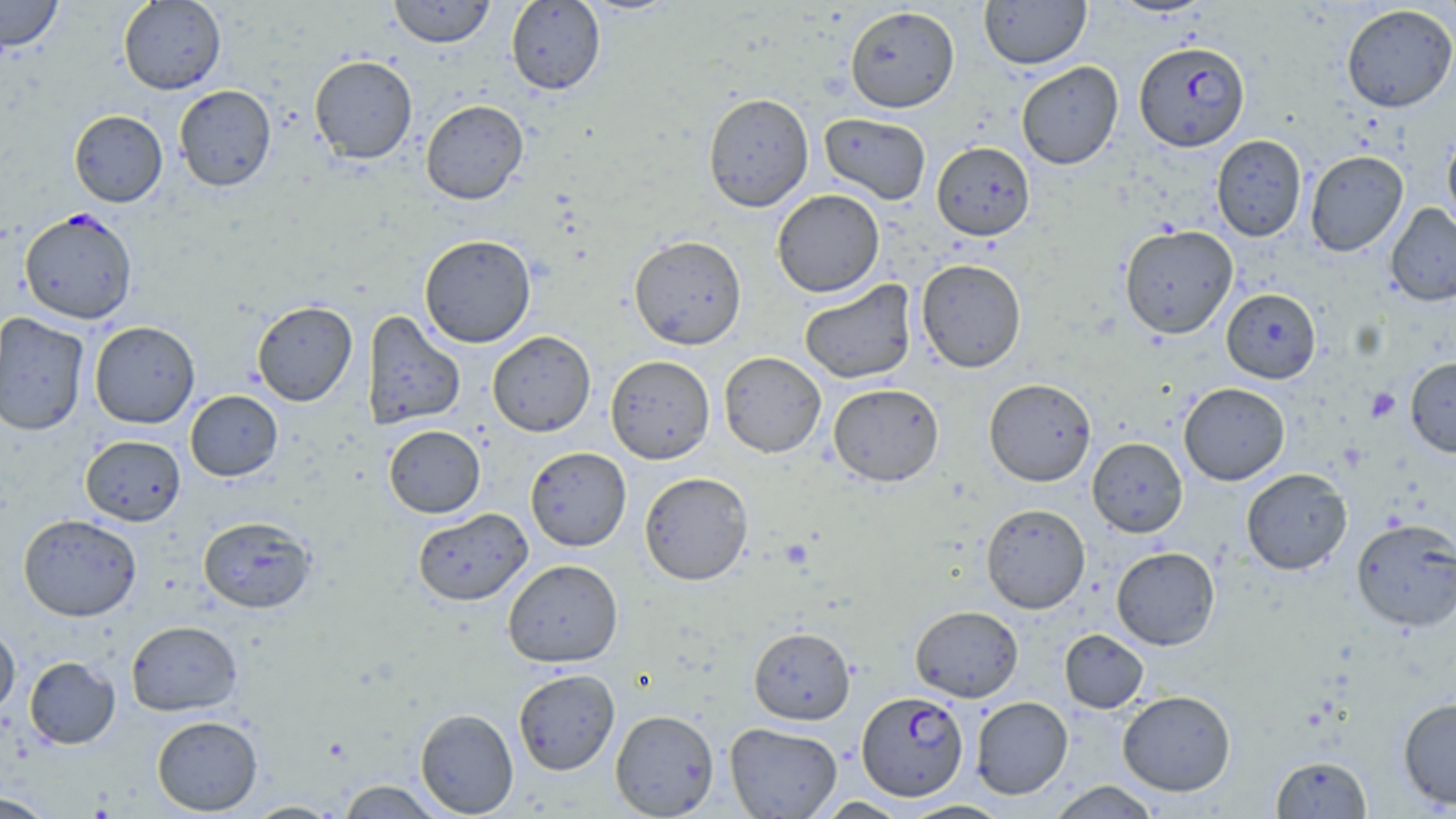

Approximate bounding boxes as [x1, y1, x2, y2] in pixels. Platelet locations: [1366, 388, 1401, 422]. Plasmodium falciparum-infected red blood cell locations: [1134, 42, 1250, 152], [19, 208, 137, 324], [856, 691, 969, 801]. Uninfected red blood cell locations: [0, 0, 63, 53], [118, 0, 226, 94], [388, 0, 496, 48], [506, 0, 606, 95], [576, 0, 683, 16], [979, 0, 1091, 69], [1108, 0, 1215, 18], [1439, 0, 1456, 39], [1341, 4, 1455, 113], [845, 6, 960, 113], [309, 55, 418, 164], [1016, 61, 1123, 169], [173, 85, 277, 192], [703, 92, 814, 212], [420, 99, 529, 204], [69, 110, 167, 207], [819, 113, 931, 204], [1442, 128, 1456, 232], [1211, 135, 1307, 241], [931, 141, 1034, 239], [1305, 150, 1408, 256], [772, 189, 884, 297], [1386, 203, 1456, 306], [1119, 225, 1238, 339], [419, 234, 536, 348], [628, 235, 747, 350], [916, 258, 1027, 373], [799, 279, 916, 384], [1221, 288, 1321, 383], [251, 300, 357, 406], [362, 310, 466, 430], [0, 313, 90, 437], [89, 321, 200, 428], [487, 330, 596, 437], [719, 351, 826, 458], [605, 355, 715, 464], [1405, 357, 1456, 457], [984, 378, 1096, 486], [1179, 382, 1290, 485], [828, 383, 944, 487], [185, 390, 282, 481], [384, 425, 485, 517], [80, 435, 186, 525], [1087, 437, 1187, 537], [525, 446, 631, 551], [1241, 468, 1352, 575], [639, 471, 753, 585], [981, 503, 1091, 614], [413, 508, 532, 605], [18, 514, 142, 621], [198, 516, 317, 614], [1351, 518, 1456, 632], [1111, 546, 1220, 650], [502, 558, 624, 668], [910, 605, 1024, 702], [126, 620, 243, 716], [0, 625, 20, 716], [748, 626, 855, 724], [1060, 629, 1148, 713], [24, 656, 120, 749], [513, 668, 620, 775], [1117, 690, 1236, 796], [971, 696, 1072, 799], [1398, 697, 1456, 810], [415, 708, 518, 817], [610, 709, 719, 818], [152, 715, 263, 815], [724, 722, 842, 818], [1271, 755, 1372, 818], [337, 780, 445, 818], [1047, 781, 1162, 818], [0, 791, 57, 818], [814, 797, 910, 818], [900, 800, 1012, 818], [244, 801, 344, 818]. Slide-level diagnosis: Plasmodium falciparum. Optical microscopy. Thin blood smear. Captured at 1000x magnification. Single field of view. May-Grünwald-Giemsa stain. Image is 1456×819 pixels.